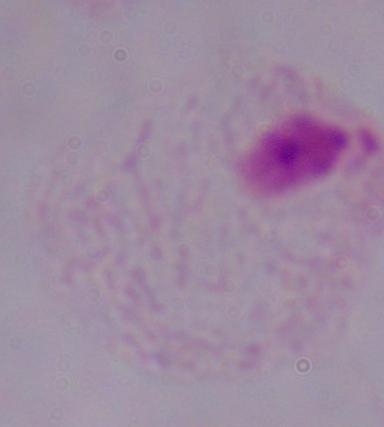
Summary:
  - Identification: trichomonad
  - Magnification: 1000x
  - Modality: photomicrograph